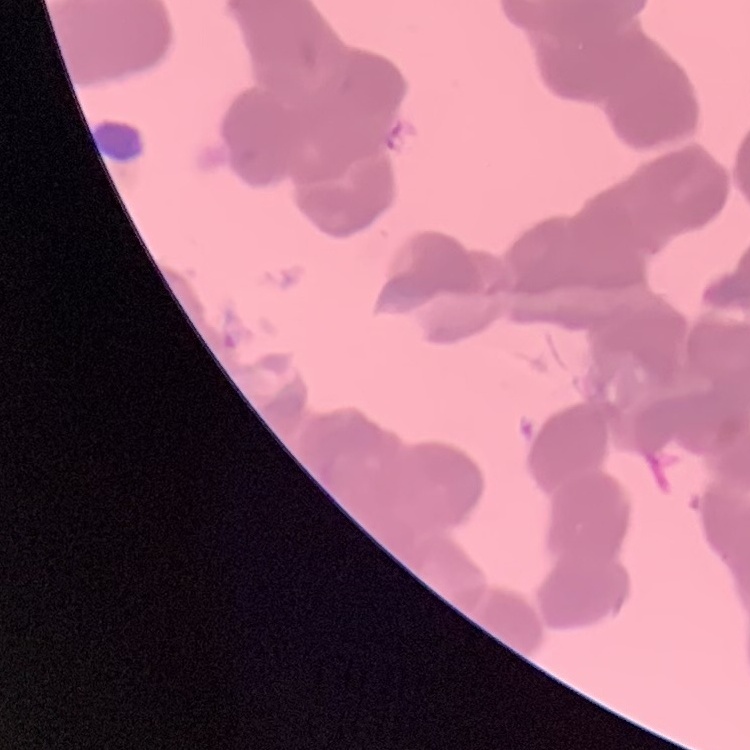 The erythrocytes exhibit rouleaux formation. Stained with either Field's or Giemsa. Thin blood smear. Square crop of a larger photomicrograph.